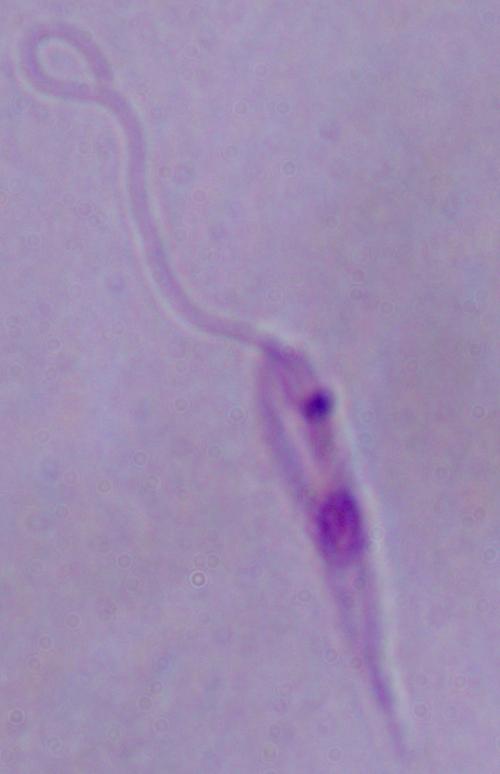 A Leishmania parasite is seen. Captured at 1000x magnification. Micrograph.